Classify this cell by malaria status.
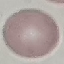

It is uninfected.

Giemsa stain. Thin blood film. Cell patch, automatically extracted from a larger field of view and resized to 64 × 64 pixels. Photographed with a smartphone camera at the microscope eyepiece.